Locate and identify every blood parasite.
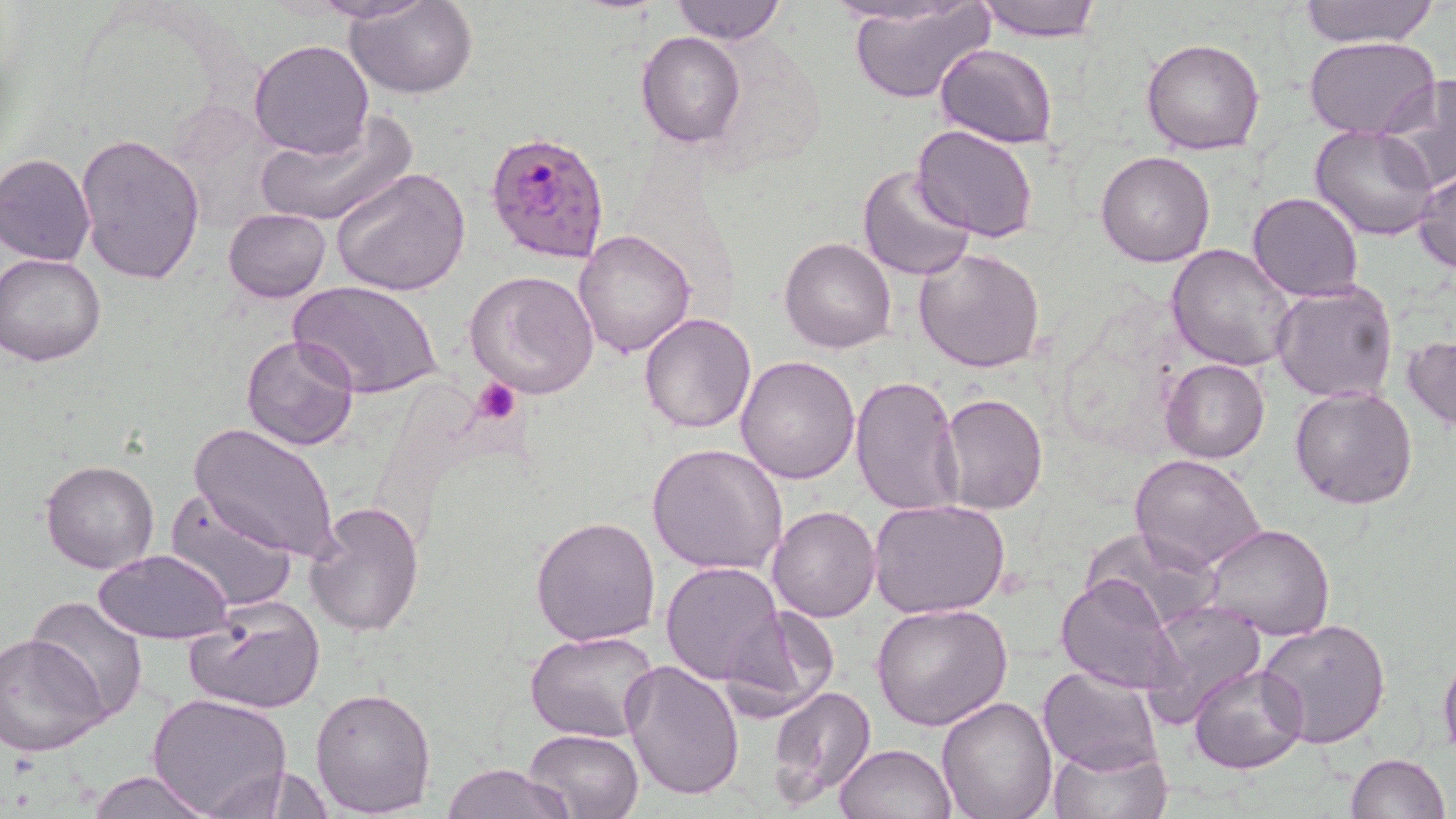

Approximate bounding boxes as (x1, y1, x2, y2) in pixels.
Plasmodium falciparum-infected red blood cells: (483, 127, 613, 267).
No Plasmodium ovale, Plasmodium malariae, Plasmodium vivax, Babesia divergens, or Trypanosoma brucei observed.

Platelet locations: (472, 378, 522, 425). Uninfected red blood cell locations: (309, 0, 434, 25), (671, 0, 785, 45), (973, 0, 1102, 41), (1297, 0, 1438, 48), (346, 1, 477, 98), (826, 1, 977, 28), (849, 2, 995, 104), (635, 31, 746, 149), (1303, 35, 1441, 138), (1141, 37, 1266, 156), (249, 38, 375, 159), (934, 43, 1058, 148), (1377, 75, 1456, 195), (254, 111, 416, 228), (914, 124, 1039, 241), (1309, 125, 1439, 241), (74, 133, 205, 287), (1096, 149, 1216, 268), (1, 152, 97, 267), (858, 165, 977, 281), (330, 166, 472, 297), (1414, 167, 1455, 276), (1247, 192, 1364, 301), (223, 207, 332, 304), (573, 229, 696, 358), (780, 238, 897, 353), (1166, 244, 1299, 372), (914, 247, 1043, 372), (0, 252, 110, 366), (464, 270, 600, 399), (288, 279, 444, 400), (1271, 280, 1399, 405), (639, 314, 756, 434), (1405, 333, 1455, 435), (241, 334, 359, 453), (734, 355, 860, 483), (1160, 359, 1269, 463), (849, 374, 963, 518), (1290, 386, 1419, 509), (939, 393, 1048, 513), (190, 421, 341, 560), (646, 443, 789, 575), (1130, 454, 1267, 574), (42, 458, 160, 574), (164, 488, 298, 612), (867, 499, 1012, 620), (303, 501, 425, 637), (766, 505, 881, 622), (530, 515, 661, 647), (1083, 525, 1221, 633), (1203, 526, 1333, 641), (94, 549, 235, 643), (660, 560, 783, 683), (1055, 573, 1185, 696), (26, 595, 148, 725), (186, 595, 325, 716), (1143, 600, 1266, 720), (871, 603, 1012, 731), (715, 604, 839, 722), (1256, 620, 1390, 750), (526, 631, 660, 744), (2, 634, 110, 758), (1438, 647, 1456, 761), (621, 660, 745, 802), (1189, 663, 1308, 774), (1038, 666, 1163, 775), (310, 685, 437, 815), (768, 687, 878, 807), (146, 693, 292, 816), (936, 696, 1058, 818), (524, 727, 645, 819), (1048, 738, 1171, 819), (834, 744, 956, 819), (1345, 751, 1450, 819), (439, 764, 575, 819), (87, 771, 219, 818). Slide-level diagnosis: Plasmodium falciparum. Image is 1456×819 pixels. 1000x magnification. Thin blood smear. May-Grünwald-Giemsa stain. One field of a larger specimen. Light microscopy.